Locate every Plasmodium parasite and every leukocyte.
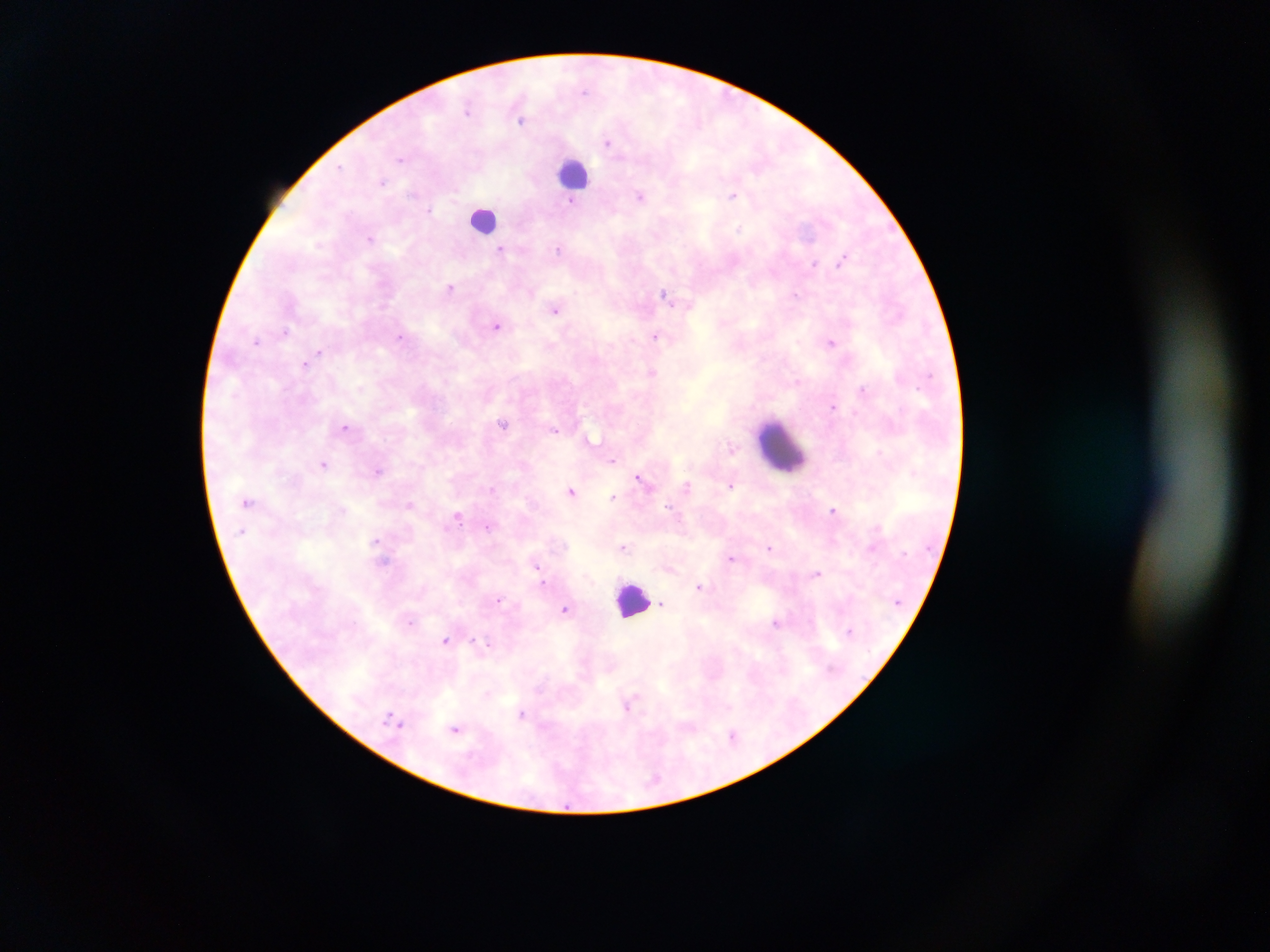

Approximate centers as [x, y] in pixels.
Plasmodium parasites: [467, 109], [521, 122], [608, 142], [400, 159], [340, 166], [382, 181], [731, 195], [641, 196], [570, 202], [429, 209], [739, 229], [370, 238], [558, 249], [500, 250], [842, 260], [814, 263], [450, 288], [665, 293], [794, 294], [556, 310], [497, 326], [286, 331], [655, 335], [399, 338], [256, 341], [831, 343], [319, 352], [305, 364], [653, 373], [862, 389], [833, 406], [503, 424], [345, 426], [556, 430], [591, 438], [731, 447], [881, 452], [612, 461], [323, 464], [378, 470], [638, 478], [731, 485], [687, 486], [492, 489], [571, 491], [613, 496], [410, 505], [668, 507], [833, 510], [458, 515], [488, 527], [877, 528], [375, 541], [623, 547], [769, 547], [872, 547], [731, 558], [384, 561], [537, 566], [817, 574], [542, 582], [699, 586], [499, 600], [662, 603], [565, 608], [411, 622], [776, 622], [445, 640], [488, 645], [628, 705], [522, 713], [390, 716], [394, 720], [401, 725], [455, 728], [732, 735].
Leukocytes: [575, 173], [482, 218], [782, 447], [632, 600].

Summary:
  - Field of view: single
  - Preparation: thick blood film
  - Capture: mobile-phone photograph through a microscope
  - Country: Ghana
  - Image size: 1270×952 pixels